Comment on the morphology of the erythrocytes.
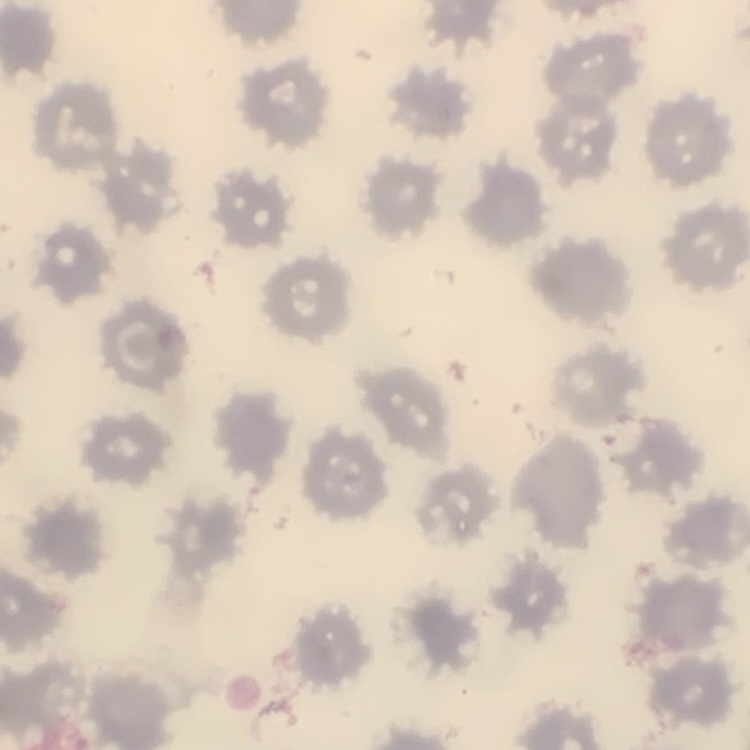
No rouleaux formation.

Summary:
  - Stain: Field's or Giemsa
  - Preparation: thin peripheral smear
  - Image type: square crop of a larger photomicrograph